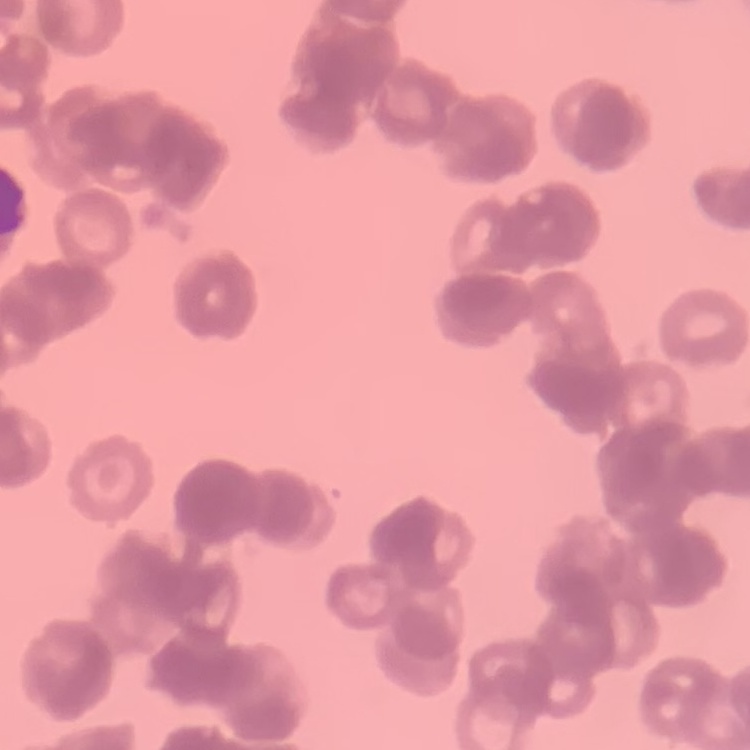
The erythrocytes exhibit rouleaux formation. One tile cut from a larger photomicrograph. Thin blood film. Stained with either Field's or Giemsa.